Name the parasite shown.
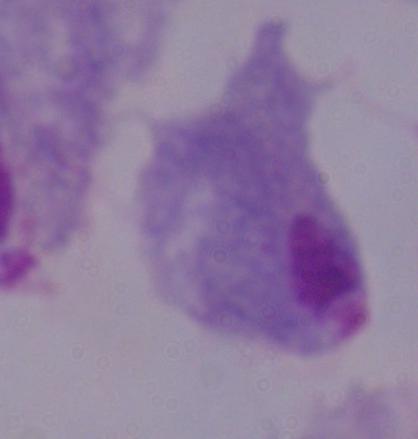
A trichomonad.

magnification = 1000x
modality = photomicrograph